Outline each blood parasite and name the species.
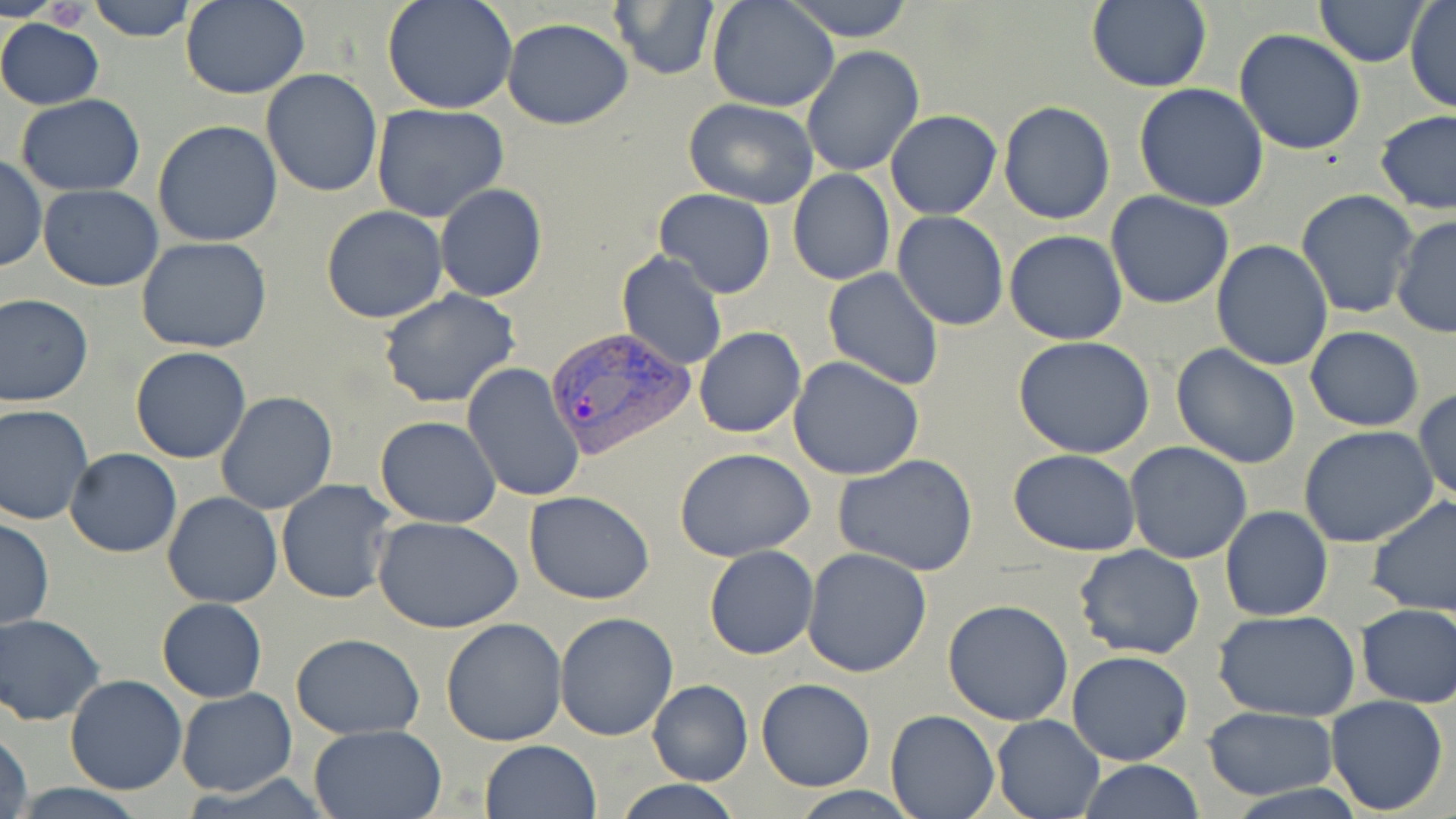
Approximate bounding boxes as [x1, y1, x2, y2] in pixels.
Plasmodium vivax-infected red blood cells: [543, 332, 694, 467].
No Plasmodium falciparum, Plasmodium ovale, Plasmodium malariae, Babesia divergens, or Trypanosoma brucei observed.

slide-level diagnosis = Plasmodium vivax
stain = May-Grünwald-Giemsa
field of view = single
magnification = 1000x
uninfected red blood cell locations = approximate bounding boxes as [x1, y1, x2, y2] in pixels: [89, 0, 198, 41], [179, 0, 311, 100], [381, 0, 518, 115], [708, 0, 839, 112], [782, 0, 918, 42], [1314, 0, 1431, 66], [609, 1, 718, 80], [1084, 1, 1212, 91], [1405, 1, 1455, 114], [0, 18, 104, 110], [503, 18, 633, 130], [1234, 29, 1368, 155], [801, 45, 925, 178], [261, 68, 383, 195], [1134, 84, 1270, 212], [15, 94, 145, 197], [683, 98, 820, 208], [998, 100, 1115, 223], [371, 104, 512, 222], [1374, 109, 1456, 215], [885, 110, 1001, 219], [152, 120, 283, 248], [0, 156, 46, 273], [788, 168, 894, 286], [435, 183, 548, 303], [39, 184, 163, 291], [1296, 189, 1419, 319], [654, 190, 776, 298], [1104, 192, 1234, 311], [321, 205, 449, 323], [893, 211, 1009, 330], [1391, 214, 1456, 342], [1004, 230, 1128, 344], [137, 237, 273, 353], [1210, 239, 1334, 371], [615, 251, 728, 371], [822, 267, 945, 390], [377, 289, 521, 408], [0, 292, 94, 408], [694, 326, 806, 438], [1305, 326, 1425, 432], [1012, 336, 1155, 459], [1170, 342, 1302, 468], [130, 346, 252, 464], [789, 358, 925, 479], [461, 363, 584, 504], [1412, 389, 1455, 505], [215, 390, 340, 514], [0, 403, 95, 525], [375, 416, 502, 527], [1300, 426, 1441, 548], [1125, 442, 1252, 565], [675, 448, 816, 563], [65, 449, 182, 557], [1009, 449, 1141, 558], [833, 453, 979, 576], [276, 480, 399, 605], [524, 489, 655, 604], [162, 493, 283, 608], [1367, 495, 1456, 619], [1222, 506, 1333, 621], [373, 516, 524, 635], [0, 518, 54, 630], [1074, 545, 1204, 660], [703, 546, 818, 660], [803, 548, 933, 678], [157, 599, 268, 702], [942, 599, 1073, 725], [1354, 603, 1456, 707], [1212, 609, 1362, 721], [553, 611, 678, 742], [1, 613, 105, 725], [440, 616, 568, 746], [291, 634, 424, 739], [22, 646, 140, 782], [1067, 650, 1195, 766], [64, 675, 187, 795], [755, 678, 875, 791], [645, 680, 754, 786], [177, 688, 298, 797], [1324, 694, 1450, 816], [1202, 707, 1338, 799], [886, 709, 999, 819], [992, 713, 1104, 819], [308, 723, 447, 818], [1, 724, 34, 819], [478, 739, 602, 819], [1079, 760, 1204, 818], [613, 780, 745, 819], [9, 782, 150, 819], [784, 787, 924, 818]
image size = 1456×819 pixels
preparation = thin blood film
modality = light microscopy